Give the extent of all uninfected red blood cells.
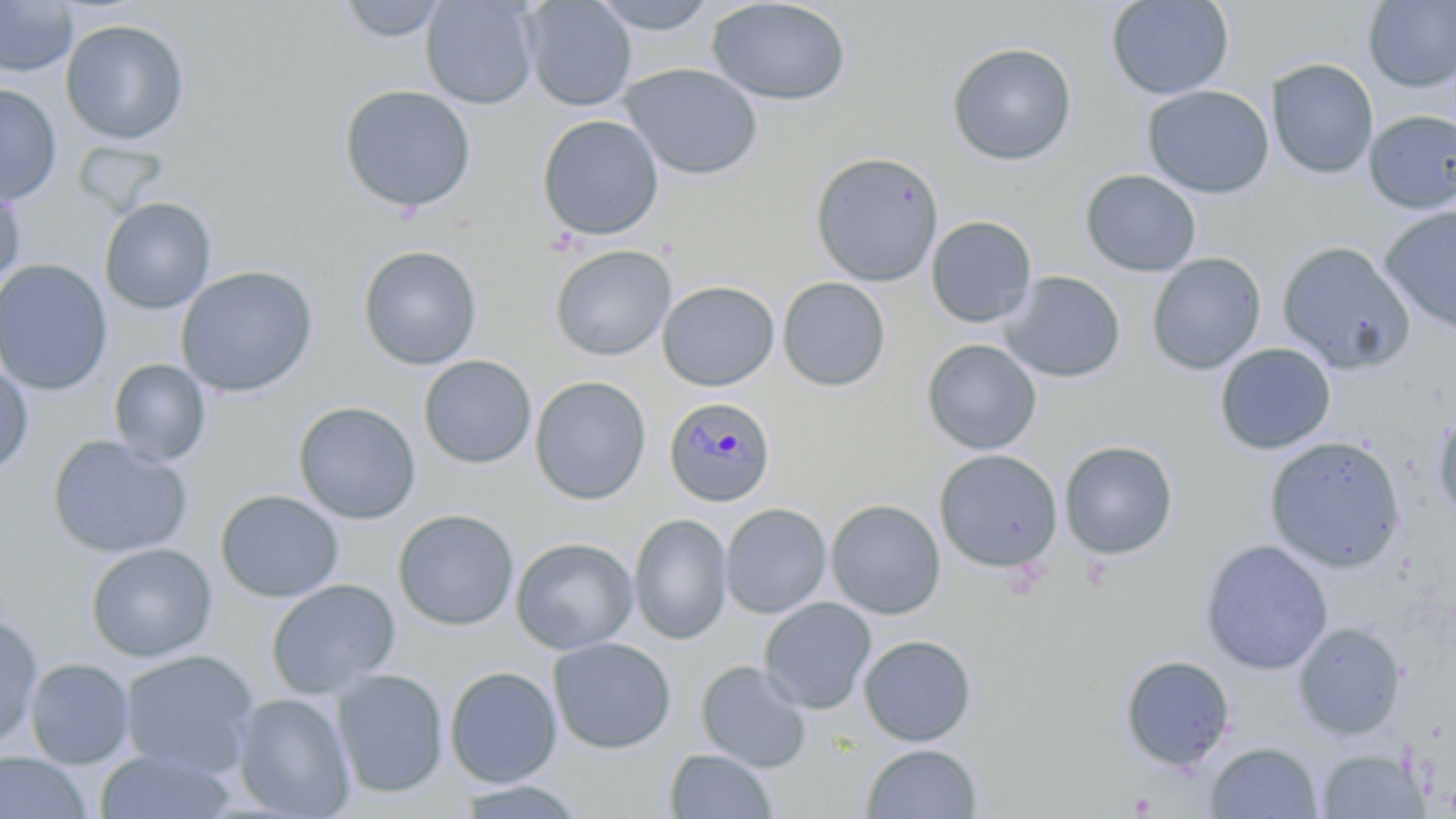
Approximate bounding boxes as [x1, y1, x2, y2] in pixels.
Uninfected red blood cells: [336, 0, 449, 43], [420, 0, 540, 110], [521, 0, 637, 111], [587, 0, 720, 35], [706, 0, 853, 106], [1105, 0, 1235, 101], [0, 1, 78, 77], [1362, 1, 1456, 92], [60, 19, 189, 144], [946, 41, 1078, 166], [1266, 59, 1379, 180], [619, 62, 764, 180], [0, 83, 62, 206], [338, 84, 477, 213], [1142, 85, 1275, 199], [1363, 110, 1456, 214], [537, 114, 664, 242], [809, 150, 945, 287], [1080, 169, 1202, 276], [0, 183, 26, 293], [99, 197, 216, 314], [1379, 204, 1456, 337], [925, 216, 1038, 328], [1277, 240, 1416, 374], [549, 244, 676, 361], [357, 245, 482, 371], [1147, 253, 1266, 374], [0, 258, 113, 396], [176, 265, 319, 397], [999, 271, 1126, 383], [777, 276, 891, 392], [656, 280, 779, 392], [921, 339, 1042, 455], [1214, 342, 1336, 455], [418, 355, 537, 469], [108, 358, 211, 465], [0, 362, 34, 477], [529, 376, 651, 506], [293, 401, 421, 524], [1430, 406, 1456, 525], [47, 435, 194, 560], [1264, 436, 1406, 572], [1059, 440, 1178, 560], [934, 449, 1063, 573], [215, 489, 344, 603], [825, 498, 946, 619], [720, 502, 832, 618], [392, 509, 519, 631], [628, 513, 732, 644], [511, 536, 639, 655], [1200, 540, 1333, 675], [85, 542, 217, 662], [265, 579, 400, 700], [758, 597, 877, 714], [0, 614, 43, 750], [1293, 622, 1406, 741], [858, 634, 977, 746], [548, 637, 676, 754], [119, 649, 260, 777], [1119, 655, 1235, 772], [23, 658, 135, 769], [695, 659, 812, 771], [444, 665, 562, 788], [331, 668, 449, 799], [230, 693, 355, 818], [1205, 742, 1323, 818], [861, 743, 982, 819], [94, 746, 236, 819], [664, 748, 779, 819], [1315, 749, 1428, 818], [0, 751, 93, 819], [453, 779, 589, 818].

Summary:
  - Plasmodium malariae-infected red blood cell locations: [664, 396, 776, 508]
  - Slide-level diagnosis: Plasmodium malariae
  - Field of view: one of a larger specimen
  - Modality: light microscopy
  - Image size: 1456×819 pixels
  - Magnification: 1000x
  - Preparation: thin blood smear
  - Stain: May-Grünwald-Giemsa